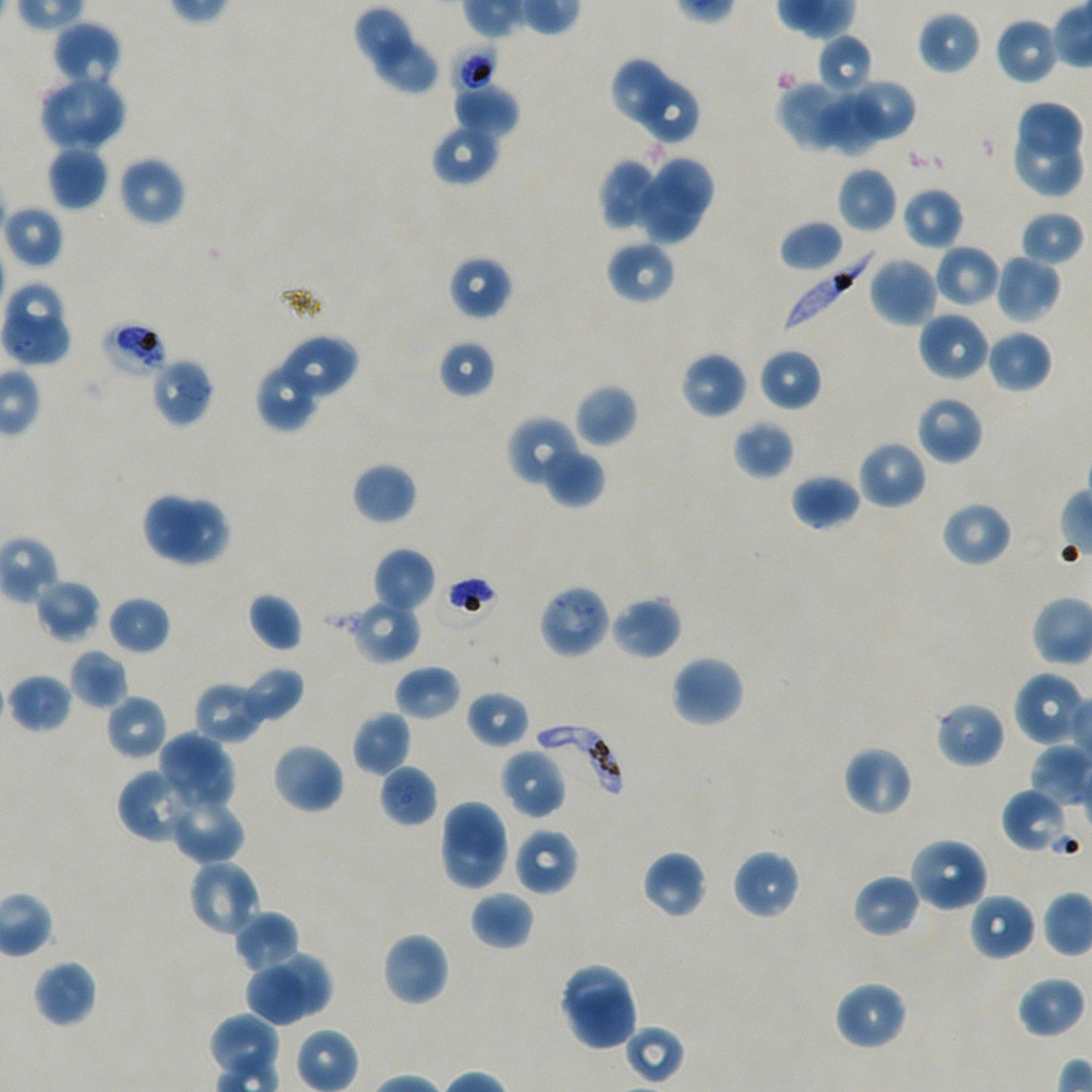
Approximate bounding boxes as (x1, y1, x2, y2) in pixels. Not every red blood cell is marked.
Summary:
  - Locations of infected red blood cells: (784, 248, 876, 335), (536, 723, 623, 803)
  - Locations of uninfected red blood cells: (353, 6, 413, 67), (917, 10, 981, 75), (994, 17, 1059, 85), (52, 21, 122, 88), (816, 34, 874, 98), (374, 40, 439, 94), (609, 56, 672, 125), (63, 79, 124, 147), (640, 79, 699, 145), (846, 79, 917, 141), (777, 80, 860, 153), (453, 85, 520, 137), (40, 86, 91, 149), (820, 92, 884, 156), (1019, 103, 1085, 156), (431, 123, 500, 186), (1014, 132, 1082, 196), (46, 145, 108, 211), (117, 156, 186, 228), (652, 156, 714, 219), (599, 158, 656, 228), (837, 166, 898, 234), (636, 181, 702, 249), (901, 187, 964, 249), (3, 204, 65, 269), (1019, 210, 1084, 266), (779, 219, 845, 272), (606, 240, 676, 305), (934, 244, 1001, 308), (995, 252, 1062, 324), (448, 255, 512, 321), (867, 255, 939, 327), (4, 281, 66, 340), (917, 310, 990, 382), (23, 318, 71, 363), (986, 329, 1053, 393), (274, 333, 359, 402), (438, 340, 496, 398), (758, 348, 822, 412), (680, 351, 748, 420), (255, 361, 320, 432), (574, 383, 638, 447), (916, 396, 984, 465), (506, 415, 583, 489), (731, 420, 794, 480), (857, 440, 927, 511), (542, 449, 605, 508), (351, 462, 417, 525), (790, 473, 861, 530), (140, 490, 202, 561), (168, 499, 232, 566), (939, 500, 1013, 568), (373, 547, 435, 614), (33, 578, 102, 642), (247, 592, 303, 653), (610, 594, 682, 661), (107, 595, 170, 654), (348, 599, 422, 665), (69, 649, 128, 710), (670, 654, 746, 729), (394, 665, 462, 721), (238, 666, 304, 723), (1013, 671, 1088, 748), (7, 673, 73, 733), (194, 682, 268, 744), (465, 689, 530, 749), (105, 694, 168, 762), (934, 701, 1005, 769), (351, 710, 411, 776), (157, 731, 223, 793), (271, 742, 345, 815), (841, 744, 913, 818), (179, 748, 234, 812), (500, 748, 566, 819), (378, 763, 438, 828), (116, 767, 198, 845), (1002, 789, 1068, 852), (437, 799, 507, 861), (175, 803, 246, 866), (440, 826, 506, 891), (513, 828, 579, 896), (908, 836, 989, 913), (731, 849, 801, 920), (641, 850, 707, 920), (186, 858, 262, 939), (852, 873, 922, 939), (470, 891, 534, 951), (968, 892, 1036, 962), (233, 910, 300, 972), (382, 931, 450, 1006), (272, 953, 334, 1014), (32, 960, 97, 1028), (558, 962, 633, 1022), (242, 963, 308, 1027), (1015, 975, 1086, 1040), (833, 981, 908, 1051), (568, 987, 637, 1049), (208, 1012, 280, 1083), (624, 1024, 685, 1085)
  - Locations of red blood cells of indeterminate infection status: (452, 44, 498, 93), (0, 312, 51, 362), (101, 321, 168, 379), (149, 357, 215, 428), (537, 583, 612, 659)
  - Image size: 1092×1092 pixels
  - Donor blood group: A+/O+
  - Preparation: thin blood film
  - Objective: 100x, oil immersion, numerical aperture 1.45
  - Culture: in-vitro P. falciparum strain NF54, static
  - Stain: Giemsa
  - Field of view: one from this slide